State the blood parasite species.
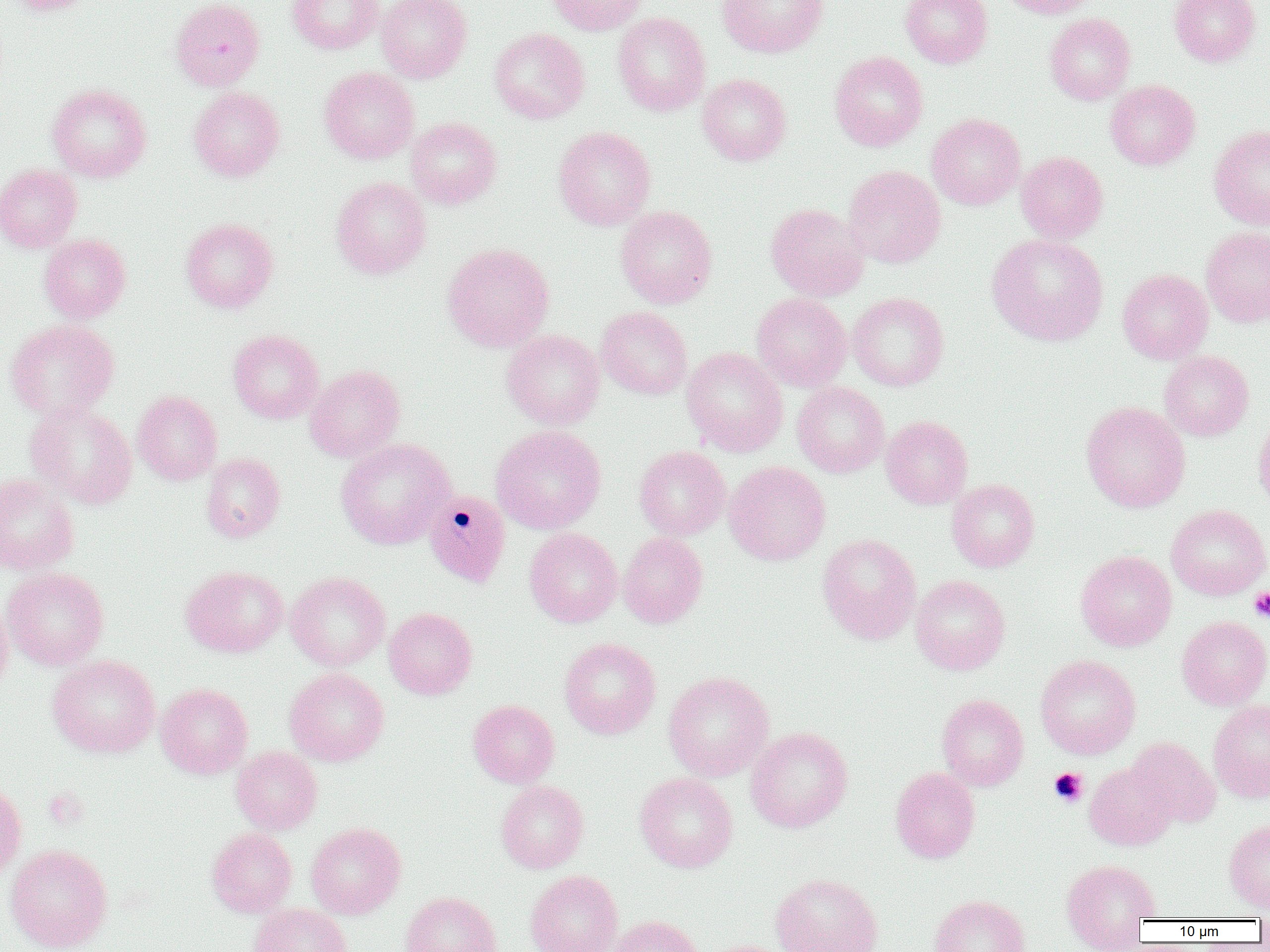

Plasmodium malariae.

Summary:
  - Coordinate format: approximate bounding boxes as (x1,y1)-(x2,y2) corner pairs in pixels
  - Plasmodium malariae-infected red blood cell locations: (423,489)-(511,587)
  - Uninfected red blood cell locations: (6,0)-(96,15), (170,0)-(264,90), (287,0)-(384,54), (376,0)-(472,83), (545,0)-(648,35), (717,0)-(828,58), (900,0)-(993,68), (995,0)-(1097,19), (1169,0)-(1261,66), (612,12)-(711,116), (1044,13)-(1136,105), (489,27)-(590,124), (829,51)-(928,151), (319,67)-(419,164), (697,73)-(791,166), (1105,80)-(1200,170), (46,83)-(151,182), (188,86)-(285,182), (926,113)-(1025,210), (405,117)-(502,209), (1209,125)-(1270,230), (553,126)-(656,230), (1016,151)-(1108,243), (0,164)-(83,253), (843,165)-(946,268), (330,177)-(431,279), (766,203)-(869,301), (615,205)-(717,308), (181,217)-(278,313), (1201,226)-(1270,328), (39,234)-(131,323), (986,234)-(1108,345), (442,242)-(554,351), (1118,268)-(1213,364), (848,292)-(949,391), (751,293)-(851,391), (595,306)-(692,399), (503,318)-(693,407), (5,320)-(119,420), (228,329)-(324,424), (501,330)-(605,430), (682,348)-(788,456), (1159,351)-(1254,441), (305,364)-(405,462), (792,382)-(890,477), (132,391)-(222,485), (25,401)-(137,509), (1081,401)-(1190,513), (1253,413)-(1270,513), (881,415)-(973,509), (490,424)-(606,534), (335,438)-(455,550), (634,445)-(730,540), (201,452)-(285,543), (724,461)-(830,566), (0,473)-(79,575), (946,479)-(1040,572), (1166,504)-(1270,600), (524,527)-(623,628), (618,532)-(708,628), (817,533)-(921,644), (1075,550)-(1176,651), (181,565)-(288,658), (2,567)-(108,670), (285,571)-(390,671), (910,575)-(1011,675), (0,595)-(13,698), (384,607)-(477,699), (1177,616)-(1270,710), (559,637)-(660,739), (48,654)-(160,758), (1035,655)-(1140,759), (284,667)-(389,766), (663,671)-(774,781), (156,683)-(253,779), (937,694)-(1028,791), (468,699)-(559,788), (1208,699)-(1270,803), (745,726)-(853,832), (1127,737)-(1221,828), (231,746)-(322,834), (1085,761)-(1178,851), (890,767)-(980,863), (634,771)-(738,873), (0,778)-(26,883), (496,780)-(589,874), (1224,820)-(1270,913), (306,822)-(406,919), (207,827)-(297,917), (5,844)-(113,952), (1061,858)-(1161,948), (525,870)-(623,952), (771,873)-(883,952), (400,891)-(501,952), (929,895)-(1030,952), (248,903)-(352,952), (608,915)-(705,952), (700,940)-(796,952)
  - Platelet locations: (1250,587)-(1270,622), (1048,767)-(1088,807)
  - Preparation: thin blood smear
  - Field of view: single
  - Image size: 1270×952 pixels
  - Modality: light microscopy
  - Magnification: 1000x